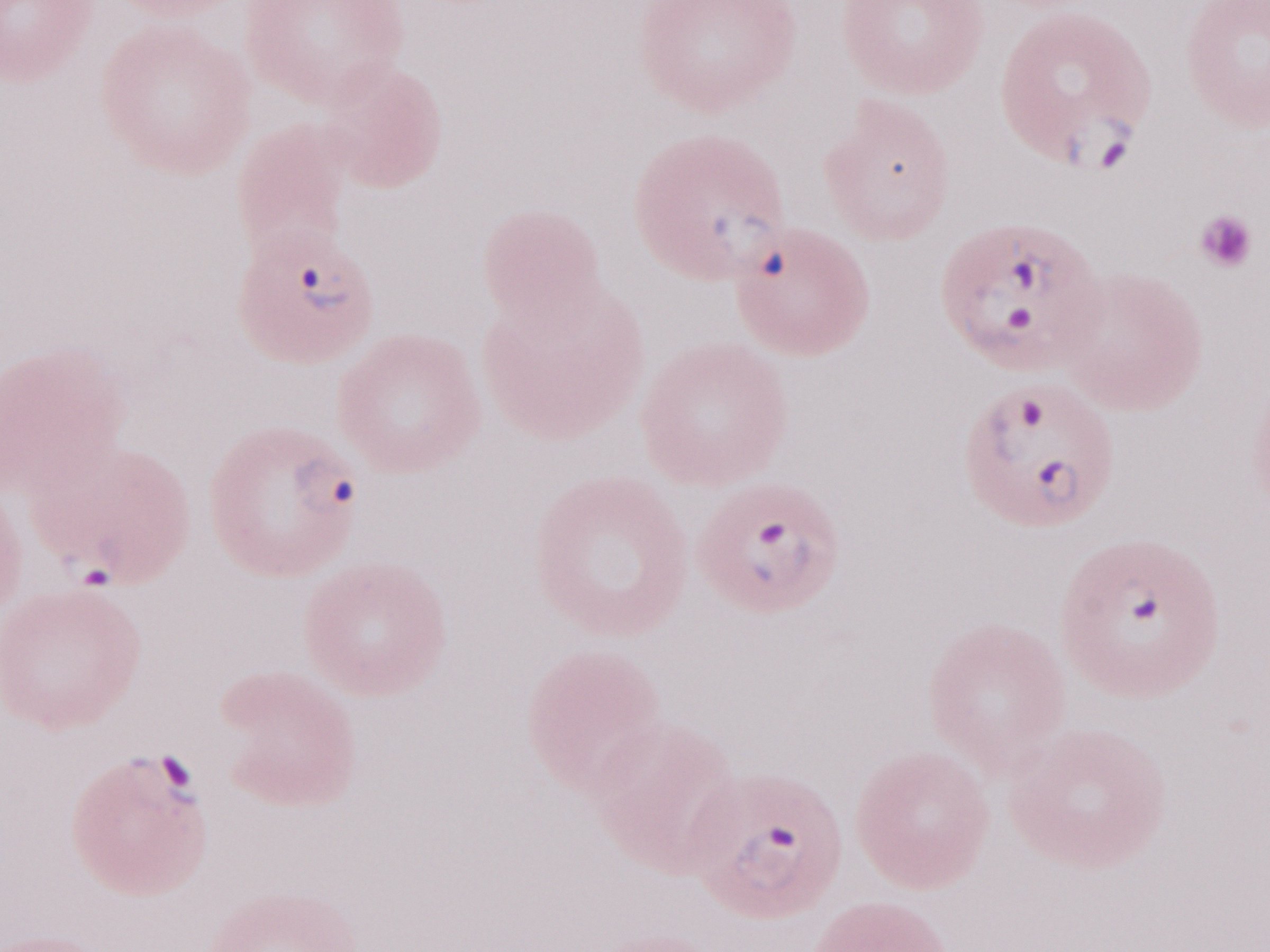
Image is 1270×952 pixels. Olympus BX43 microscope, Olympus DP73 camera. Thin peripheral-blood smear. May-Grünwald-Giemsa-stained preparation. 1,000x magnification. Patient-level malaria diagnosis: positive. Single field of view.